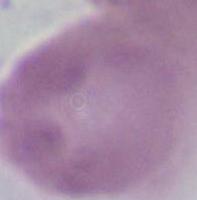
A red blood cell is shown. Captured at 1000x magnification. Micrograph.